Outline each uninfected red blood cell.
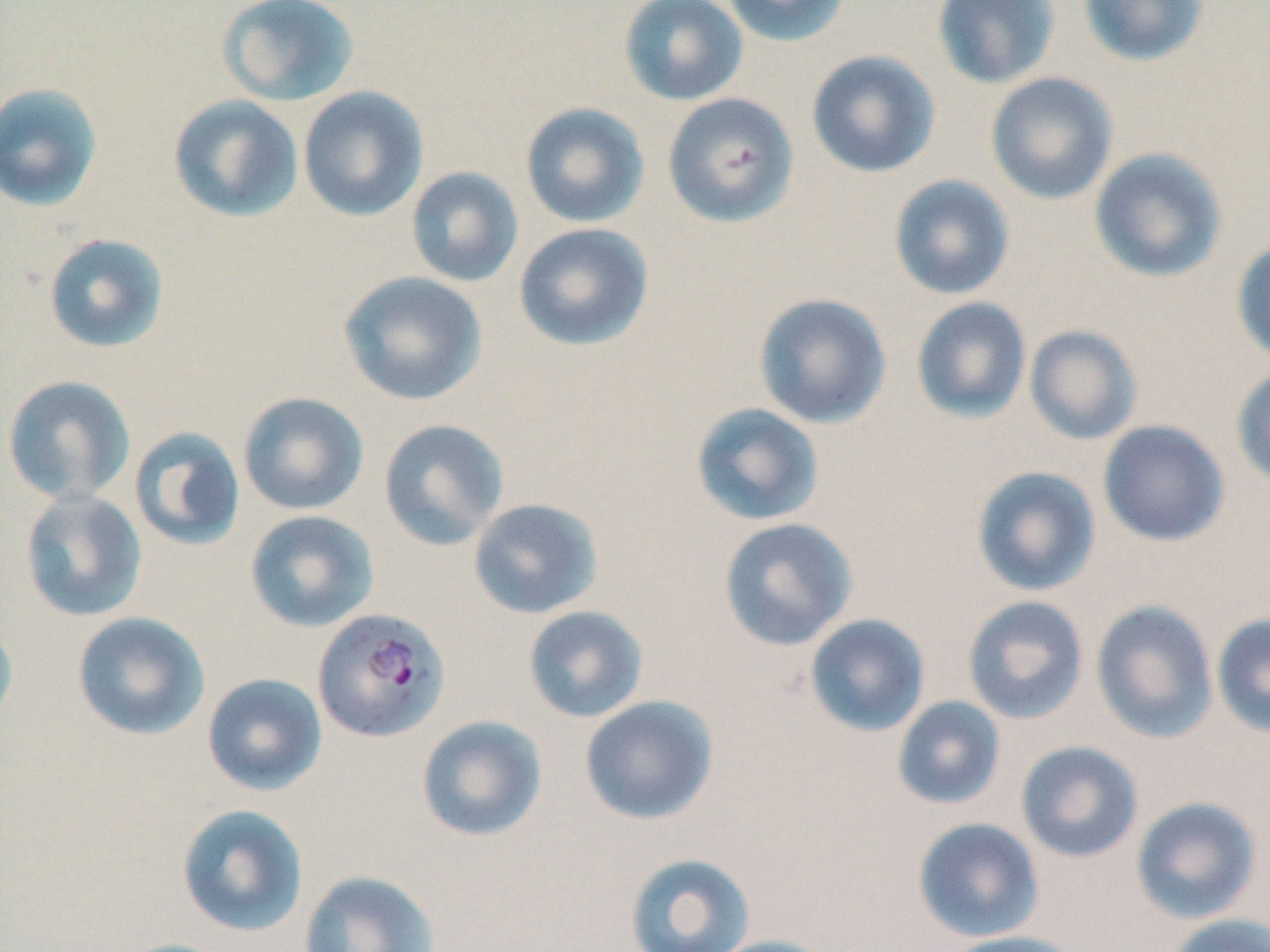

Approximate bounding boxes as [x1, y1, x2, y2] in pixels.
Uninfected red blood cells: [619, 0, 748, 106], [720, 0, 851, 48], [932, 0, 1061, 89], [1077, 0, 1211, 68], [216, 1, 360, 107], [806, 50, 941, 178], [985, 72, 1119, 204], [0, 82, 104, 213], [297, 86, 429, 222], [662, 93, 799, 228], [168, 94, 304, 223], [519, 102, 650, 228], [1089, 147, 1228, 283], [405, 167, 524, 288], [888, 174, 1016, 300], [513, 222, 654, 352], [43, 233, 170, 354], [1231, 239, 1270, 367], [338, 271, 487, 406], [753, 293, 892, 429], [910, 297, 1032, 423], [1024, 325, 1142, 445], [1231, 364, 1270, 490], [1, 375, 135, 505], [238, 391, 369, 516], [690, 402, 825, 526], [378, 419, 509, 551], [1097, 420, 1230, 547], [129, 426, 246, 551], [970, 465, 1101, 597], [19, 489, 147, 622], [467, 497, 604, 619], [244, 510, 380, 632], [718, 517, 857, 651], [962, 595, 1089, 725], [1091, 600, 1218, 743], [522, 605, 648, 723], [0, 610, 18, 738], [71, 611, 210, 741], [1211, 613, 1270, 739], [804, 614, 930, 737], [201, 672, 327, 796], [578, 695, 719, 825], [891, 696, 1006, 810], [415, 715, 547, 842], [1015, 741, 1143, 863], [1129, 797, 1263, 925], [176, 803, 309, 936], [912, 817, 1045, 943], [623, 852, 756, 952], [298, 870, 440, 952], [1165, 913, 1270, 952], [940, 930, 1085, 952], [703, 935, 837, 952], [110, 937, 237, 952].

slide-level diagnosis = Plasmodium falciparum
stain = May-Grünwald-Giemsa
Plasmodium falciparum-infected red blood cell locations = approximate bounding boxes as [x1, y1, x2, y2] in pixels: [313, 608, 449, 743]
image size = 1270×952 pixels
field of view = single
magnification = 1000x
modality = optical microscopy
preparation = thin blood film